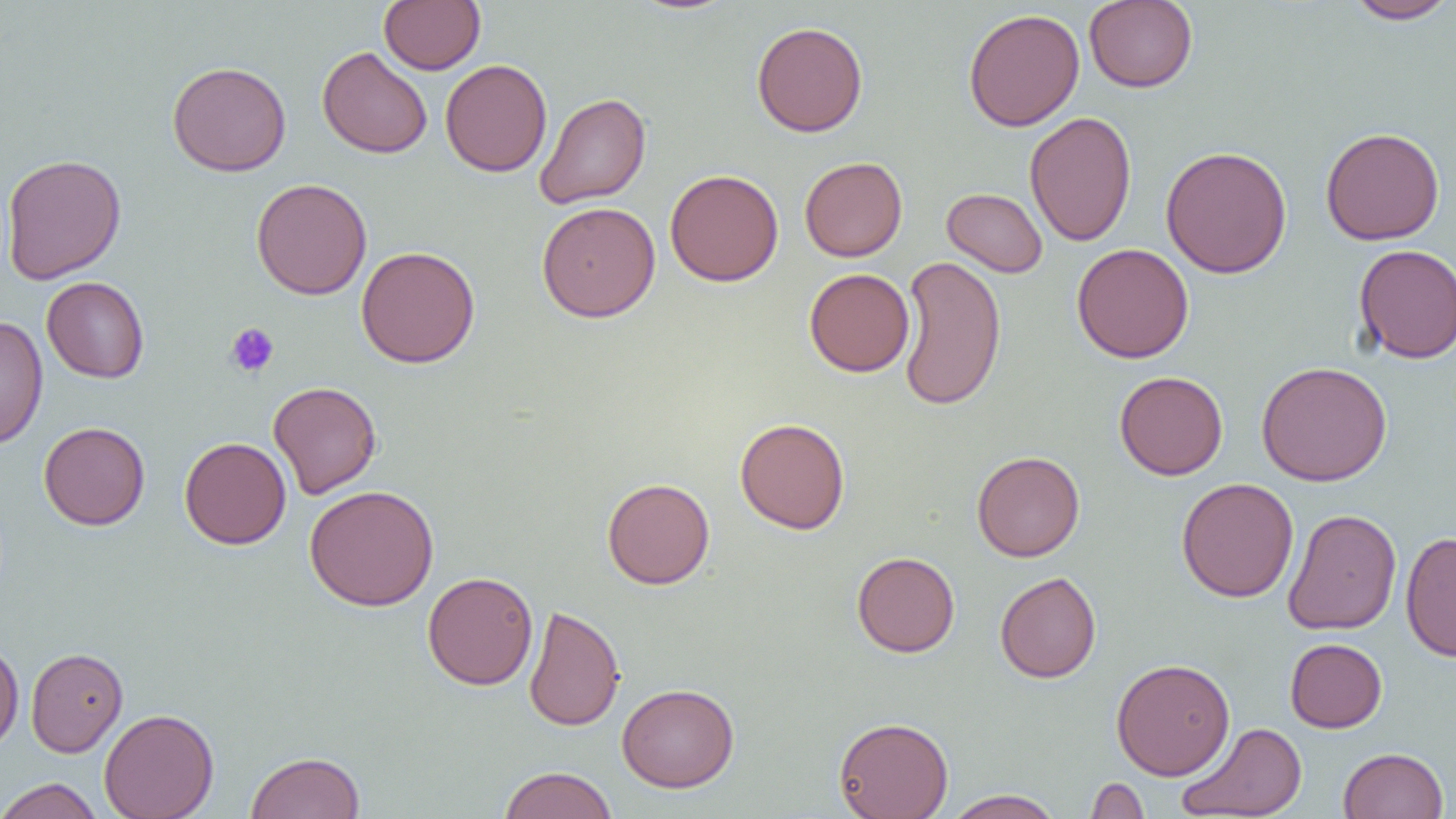
Summary:
  - Coordinate format: approximate bounding boxes as named x1/y1/x2/y2 corners in pixels
  - Platelet locations: (x1=225, y1=323, x2=279, y2=377)
  - Uninfected red blood cell locations: (x1=379, y1=0, x2=485, y2=74), (x1=1084, y1=0, x2=1198, y2=92), (x1=1344, y1=1, x2=1456, y2=24), (x1=963, y1=8, x2=1085, y2=132), (x1=751, y1=21, x2=868, y2=137), (x1=317, y1=46, x2=433, y2=159), (x1=440, y1=59, x2=552, y2=177), (x1=167, y1=61, x2=291, y2=176), (x1=534, y1=92, x2=651, y2=209), (x1=1024, y1=111, x2=1137, y2=247), (x1=1320, y1=126, x2=1445, y2=245), (x1=1160, y1=145, x2=1293, y2=279), (x1=1, y1=153, x2=126, y2=284), (x1=799, y1=156, x2=907, y2=262), (x1=665, y1=169, x2=784, y2=286), (x1=250, y1=177, x2=372, y2=300), (x1=942, y1=188, x2=1048, y2=277), (x1=536, y1=201, x2=660, y2=322), (x1=1071, y1=243, x2=1194, y2=363), (x1=1353, y1=244, x2=1456, y2=363), (x1=356, y1=245, x2=480, y2=368), (x1=897, y1=254, x2=1007, y2=412), (x1=804, y1=268, x2=914, y2=377), (x1=42, y1=276, x2=150, y2=383), (x1=0, y1=315, x2=48, y2=450), (x1=1256, y1=360, x2=1393, y2=487), (x1=1114, y1=371, x2=1228, y2=480), (x1=268, y1=381, x2=382, y2=498), (x1=735, y1=417, x2=850, y2=534), (x1=39, y1=421, x2=150, y2=530), (x1=179, y1=436, x2=291, y2=549), (x1=972, y1=450, x2=1085, y2=562), (x1=602, y1=477, x2=715, y2=589), (x1=1176, y1=477, x2=1299, y2=602), (x1=304, y1=484, x2=439, y2=611), (x1=1283, y1=508, x2=1401, y2=635), (x1=1400, y1=531, x2=1456, y2=662), (x1=852, y1=551, x2=960, y2=657), (x1=423, y1=571, x2=538, y2=690), (x1=995, y1=571, x2=1102, y2=683), (x1=523, y1=604, x2=625, y2=731), (x1=1285, y1=638, x2=1387, y2=733), (x1=0, y1=640, x2=24, y2=753), (x1=25, y1=647, x2=128, y2=757), (x1=1111, y1=658, x2=1235, y2=780), (x1=616, y1=682, x2=740, y2=792), (x1=99, y1=708, x2=219, y2=819), (x1=834, y1=716, x2=954, y2=819), (x1=1177, y1=722, x2=1307, y2=818), (x1=1338, y1=747, x2=1448, y2=819), (x1=245, y1=751, x2=365, y2=819), (x1=498, y1=765, x2=618, y2=819), (x1=1085, y1=776, x2=1150, y2=818), (x1=0, y1=777, x2=104, y2=819), (x1=943, y1=789, x2=1064, y2=818)
  - Slide-level diagnosis: negative for blood parasites
  - Preparation: thin blood film
  - Image size: 1456×819 pixels
  - Field of view: single
  - Modality: light microscopy
  - Magnification: 1000x